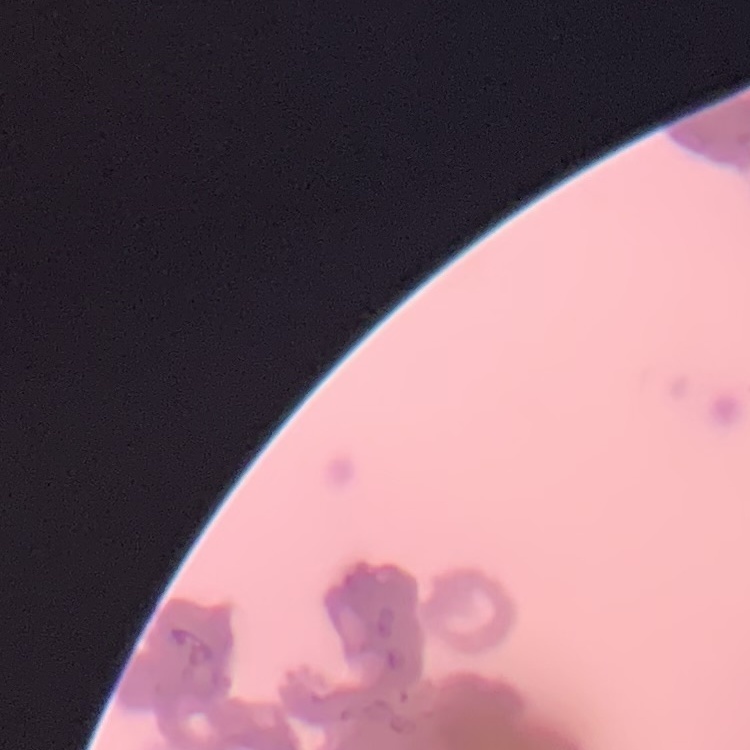

erythrocyte morphology = rouleaux formation
preparation = thin peripheral smear
image type = one tile cut from a larger photomicrograph
stain = Field's or Giemsa